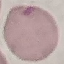

malaria status = uninfected
capture = smartphone camera at the microscope eyepiece
image type = cell patch, automatically extracted from a larger field of view and resized to 64 × 64 pixels
preparation = thin blood film
stain = Giemsa